Identify the blood parasite species.
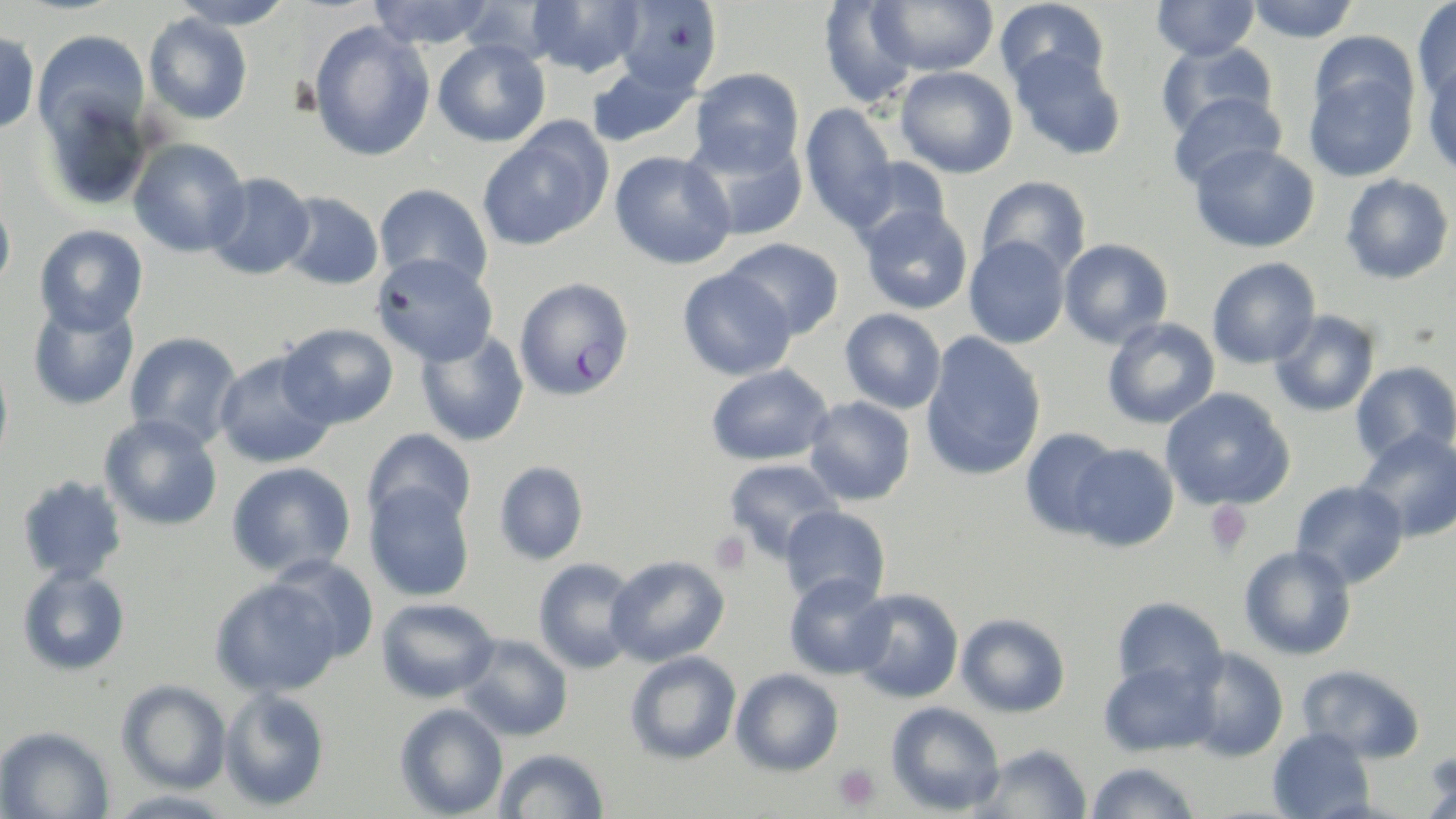

Plasmodium falciparum.

Summary:
  - Coordinate format: approximate bounding boxes as named x1/y1/x2/y2 corners in pixels
  - Plasmodium falciparum-infected red blood cell locations: (x1=513, y1=277, x2=635, y2=401)
  - Platelet locations: (x1=1205, y1=501, x2=1253, y2=555), (x1=709, y1=531, x2=752, y2=575), (x1=833, y1=763, x2=881, y2=813)
  - Uninfected red blood cell locations: (x1=168, y1=0, x2=297, y2=29), (x1=456, y1=0, x2=570, y2=65), (x1=528, y1=0, x2=647, y2=78), (x1=613, y1=0, x2=723, y2=95), (x1=869, y1=0, x2=999, y2=76), (x1=994, y1=0, x2=1109, y2=92), (x1=1151, y1=0, x2=1261, y2=61), (x1=1246, y1=0, x2=1359, y2=43), (x1=1412, y1=0, x2=1456, y2=103), (x1=367, y1=1, x2=495, y2=49), (x1=819, y1=1, x2=919, y2=108), (x1=143, y1=12, x2=254, y2=125), (x1=307, y1=21, x2=436, y2=162), (x1=0, y1=29, x2=40, y2=135), (x1=32, y1=30, x2=150, y2=141), (x1=1308, y1=31, x2=1419, y2=127), (x1=432, y1=39, x2=551, y2=147), (x1=1155, y1=41, x2=1277, y2=140), (x1=1010, y1=48, x2=1127, y2=160), (x1=585, y1=61, x2=700, y2=149), (x1=1422, y1=61, x2=1456, y2=178), (x1=895, y1=66, x2=1018, y2=178), (x1=690, y1=67, x2=804, y2=174), (x1=1304, y1=69, x2=1418, y2=181), (x1=36, y1=89, x2=154, y2=211), (x1=1168, y1=91, x2=1287, y2=190), (x1=800, y1=102, x2=899, y2=231), (x1=476, y1=128, x2=609, y2=251), (x1=684, y1=130, x2=808, y2=241), (x1=127, y1=137, x2=250, y2=258), (x1=1190, y1=142, x2=1319, y2=253), (x1=609, y1=151, x2=735, y2=269), (x1=848, y1=154, x2=952, y2=247), (x1=204, y1=172, x2=316, y2=280), (x1=1340, y1=174, x2=1454, y2=284), (x1=977, y1=175, x2=1092, y2=278), (x1=373, y1=183, x2=493, y2=289), (x1=278, y1=191, x2=384, y2=291), (x1=0, y1=194, x2=16, y2=298), (x1=859, y1=205, x2=973, y2=315), (x1=34, y1=224, x2=149, y2=336), (x1=963, y1=236, x2=1070, y2=349), (x1=723, y1=237, x2=845, y2=340), (x1=1059, y1=238, x2=1173, y2=349), (x1=372, y1=252, x2=498, y2=367), (x1=1206, y1=257, x2=1321, y2=369), (x1=677, y1=268, x2=796, y2=381), (x1=28, y1=298, x2=140, y2=410), (x1=839, y1=308, x2=946, y2=413), (x1=1269, y1=309, x2=1381, y2=417), (x1=1101, y1=317, x2=1220, y2=429), (x1=277, y1=323, x2=398, y2=430), (x1=414, y1=327, x2=530, y2=447), (x1=124, y1=331, x2=243, y2=448), (x1=921, y1=331, x2=1046, y2=481), (x1=213, y1=350, x2=338, y2=469), (x1=0, y1=353, x2=14, y2=474), (x1=1351, y1=361, x2=1455, y2=466), (x1=705, y1=363, x2=833, y2=467), (x1=1160, y1=387, x2=1295, y2=511), (x1=804, y1=396, x2=916, y2=506), (x1=99, y1=415, x2=223, y2=531), (x1=363, y1=427, x2=476, y2=531), (x1=1020, y1=428, x2=1122, y2=538), (x1=1354, y1=428, x2=1456, y2=543), (x1=1068, y1=444, x2=1180, y2=552), (x1=723, y1=458, x2=844, y2=560), (x1=226, y1=461, x2=357, y2=579), (x1=494, y1=461, x2=589, y2=564), (x1=16, y1=474, x2=129, y2=584), (x1=1291, y1=480, x2=1409, y2=589), (x1=364, y1=482, x2=475, y2=602), (x1=779, y1=505, x2=891, y2=608), (x1=1239, y1=545, x2=1357, y2=661), (x1=605, y1=554, x2=730, y2=667), (x1=266, y1=556, x2=381, y2=665), (x1=533, y1=557, x2=641, y2=674), (x1=17, y1=566, x2=131, y2=676), (x1=784, y1=573, x2=894, y2=680), (x1=209, y1=577, x2=344, y2=698), (x1=846, y1=588, x2=965, y2=703), (x1=376, y1=597, x2=499, y2=703), (x1=1112, y1=597, x2=1228, y2=696), (x1=956, y1=613, x2=1070, y2=718), (x1=458, y1=634, x2=574, y2=742), (x1=1183, y1=648, x2=1289, y2=763), (x1=624, y1=650, x2=741, y2=764), (x1=1098, y1=660, x2=1219, y2=757), (x1=1297, y1=663, x2=1425, y2=764), (x1=731, y1=668, x2=844, y2=776), (x1=116, y1=680, x2=232, y2=794), (x1=219, y1=687, x2=331, y2=812), (x1=885, y1=701, x2=1006, y2=816), (x1=394, y1=703, x2=508, y2=818), (x1=0, y1=725, x2=115, y2=818), (x1=1268, y1=729, x2=1375, y2=819), (x1=973, y1=743, x2=1093, y2=818), (x1=494, y1=748, x2=610, y2=818), (x1=1419, y1=753, x2=1456, y2=819), (x1=1084, y1=762, x2=1200, y2=818), (x1=104, y1=789, x2=237, y2=818)
  - Magnification: 1000x
  - Image size: 1456×819 pixels
  - Stain: May-Grünwald-Giemsa
  - Preparation: thin blood film
  - Modality: optical microscopy
  - Field of view: single